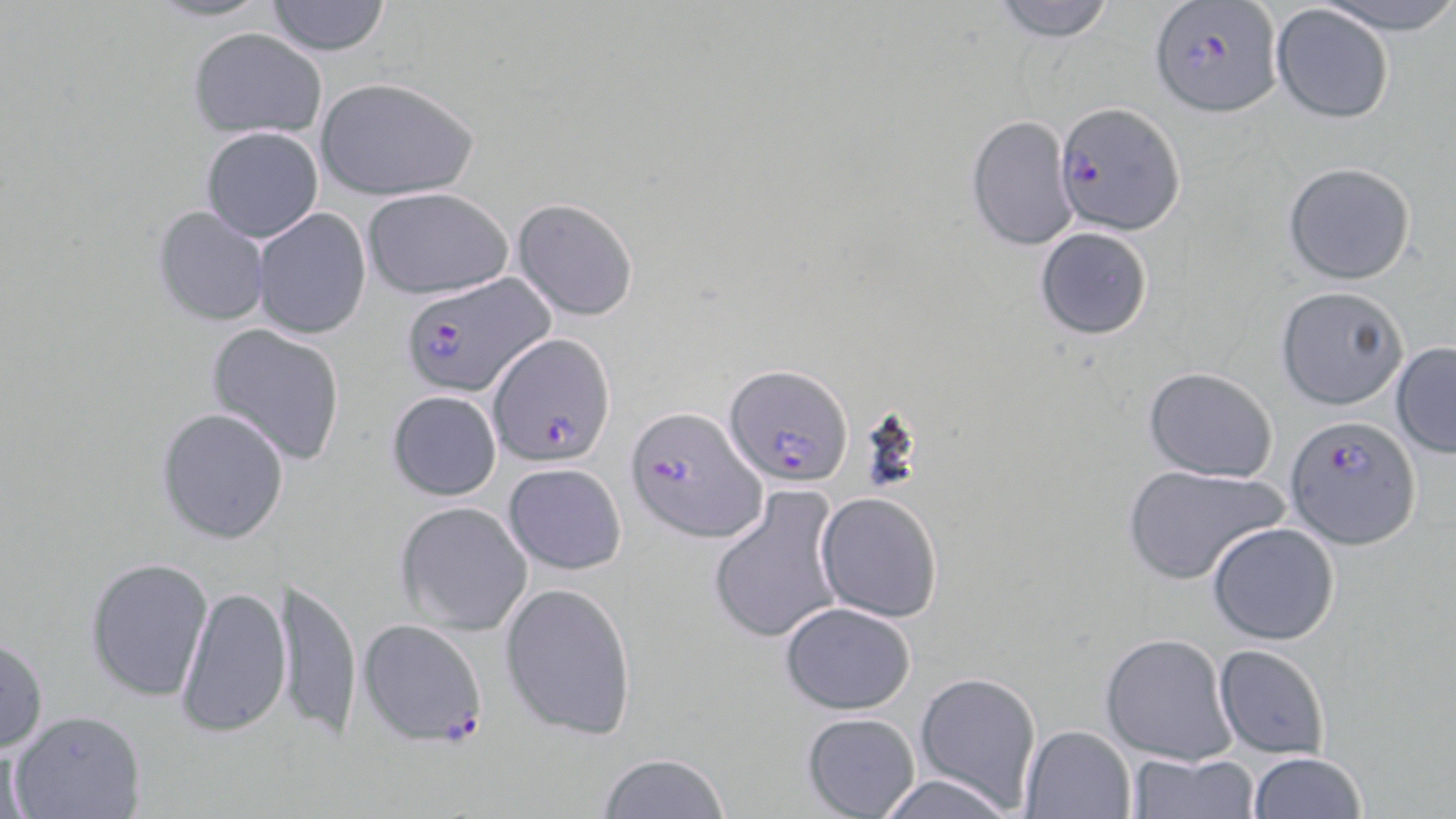
slide-level diagnosis = Plasmodium falciparum
modality = light microscopy
stain = May-Grünwald-Giemsa
field of view = one of a larger specimen
preparation = thin blood film
uninfected red blood cell locations = approximate bounding boxes as [x1, y1, x2, y2] in pixels: [141, 0, 280, 24], [989, 0, 1118, 43], [1316, 0, 1456, 32], [263, 1, 392, 56], [1271, 5, 1395, 124], [188, 27, 326, 139], [315, 77, 479, 200], [967, 114, 1077, 252], [200, 125, 324, 243], [1282, 161, 1416, 285], [361, 186, 515, 299], [510, 198, 640, 321], [152, 204, 271, 326], [252, 208, 372, 340], [1034, 227, 1152, 339], [1277, 285, 1409, 410], [205, 321, 347, 468], [1390, 342, 1456, 457], [1142, 366, 1279, 481], [386, 389, 502, 501], [156, 407, 291, 545], [502, 462, 627, 574], [1123, 463, 1289, 586], [708, 486, 846, 645], [815, 491, 944, 623], [395, 501, 532, 635], [1207, 522, 1341, 646], [85, 557, 215, 701], [276, 574, 362, 741], [499, 580, 639, 739], [177, 583, 291, 739], [779, 603, 916, 714], [1100, 632, 1234, 766], [0, 633, 49, 755], [1214, 643, 1329, 759], [915, 672, 1041, 812], [10, 710, 147, 818], [801, 711, 921, 818], [1020, 725, 1136, 818], [596, 752, 733, 819], [1126, 752, 1260, 818], [1247, 752, 1367, 818], [871, 774, 1018, 818]
magnification = 1000x
image size = 1456×819 pixels
Plasmodium falciparum-infected red blood cell locations = approximate bounding boxes as [x1, y1, x2, y2] in pixels: [1150, 1, 1285, 117], [1054, 102, 1184, 237], [397, 270, 551, 403], [489, 332, 613, 466], [725, 364, 849, 486], [626, 405, 763, 544], [1286, 415, 1419, 548], [358, 620, 488, 746]